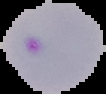

image type = cell region segmented out of the field of view; surrounding area masked to black
result = malaria parasites detected
image size = 106×94 pixels
preparation = thin blood smear